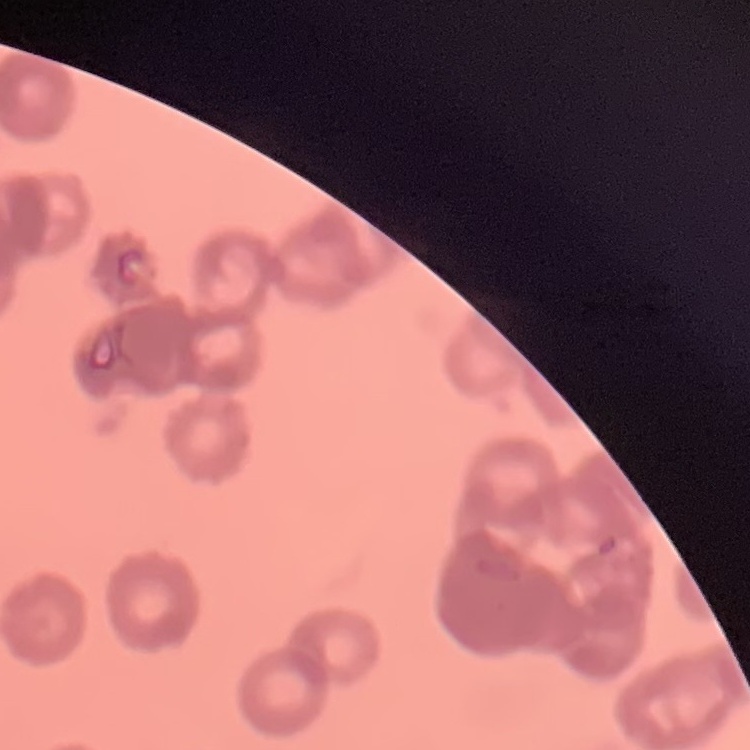 The erythrocytes exhibit rouleaux formation. Stained with either Field's or Giemsa. Thin blood film. Square crop of a larger photomicrograph.